Assess this cell for malaria.
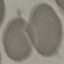

Uninfected.

Summary:
  - Preparation: thin blood film
  - Image type: automatically extracted cell patch, resized to 64 × 64 pixels
  - Stain: Giemsa
  - Capture: smartphone camera at the microscope eyepiece